Assess for malaria.
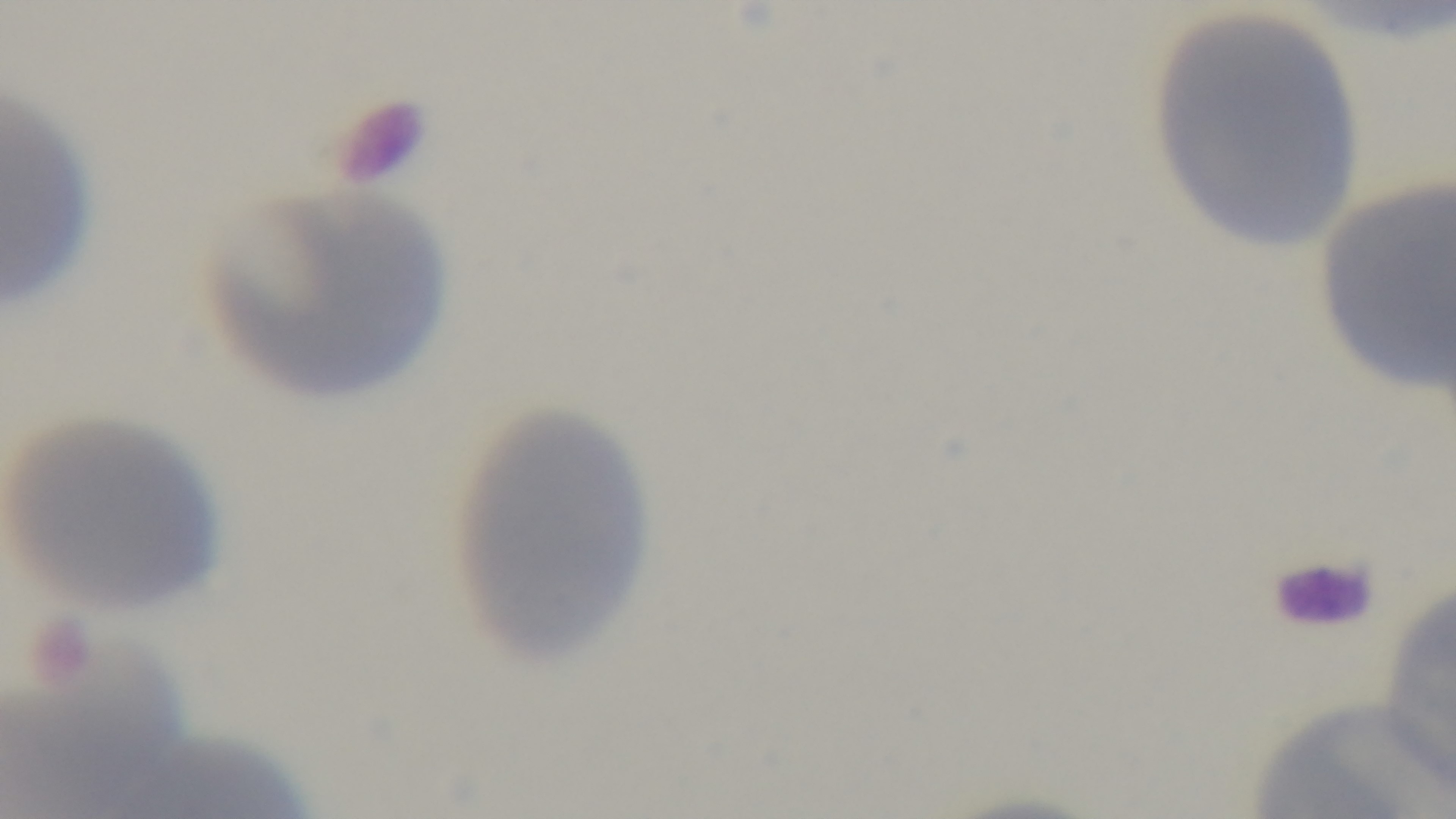
Negative.

Summary:
  - Objective: 100x oil immersion
  - Preparation: thin
  - Capture: mounted 4K digital camera
  - Modality: light microscopy
  - Field of view: single
  - Stain: Giemsa